Assess this cell for malaria.
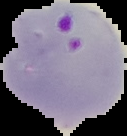

Parasitized.

Image is 127×136 pixels. Cell region segmented out of the field of view; the surrounding area is masked to black. From a thin blood film.